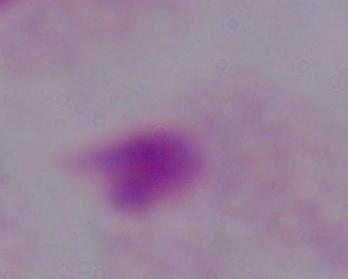
Summary:
  - Identification: trichomonad
  - Magnification: 1000x
  - Modality: photomicrograph